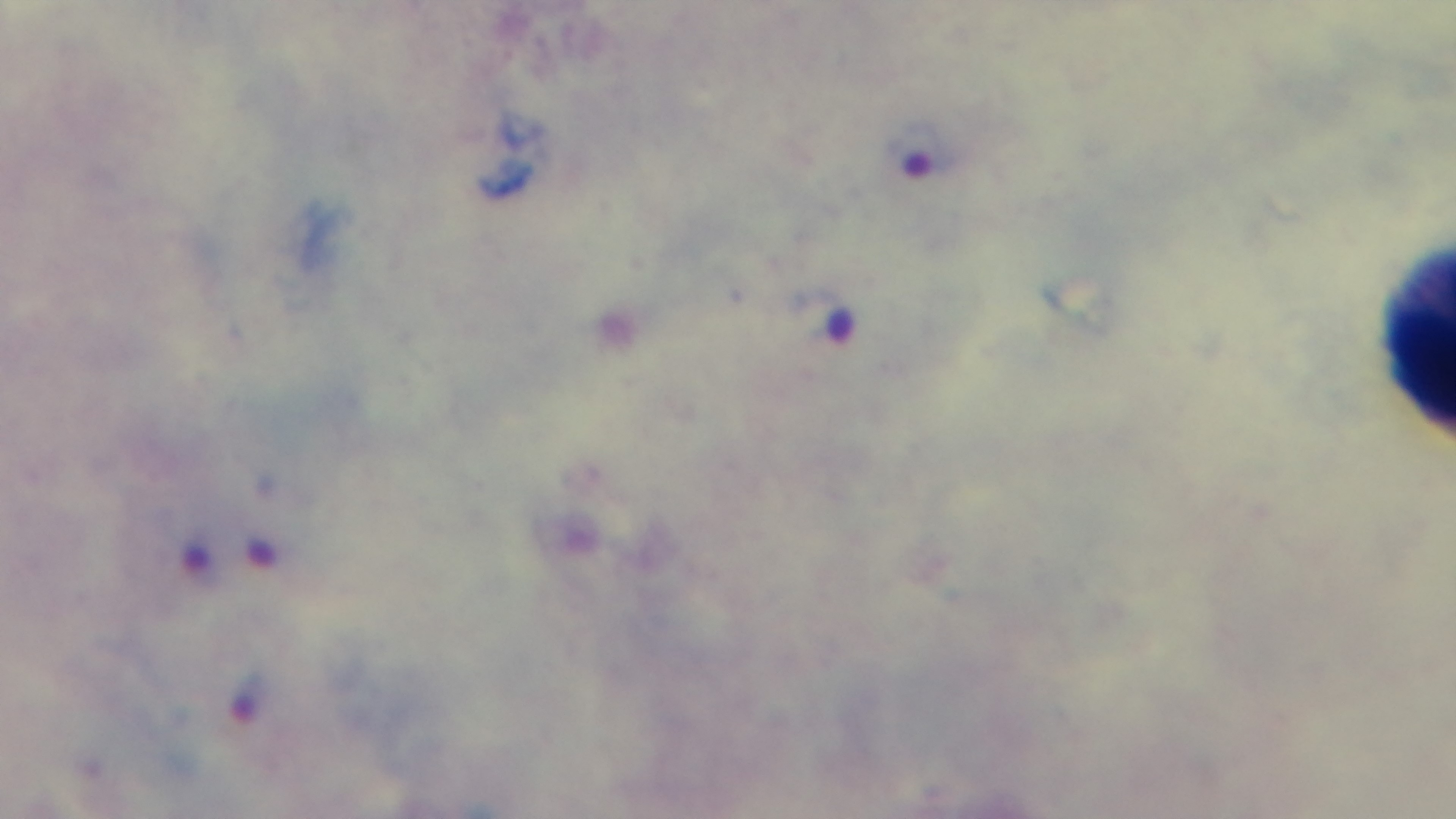
modality = light microscopy
preparation = thick blood film
objective = 100x oil immersion
field of view = one from the slide
capture = mounted 4K digital camera
malaria status = infected
stain = Giemsa